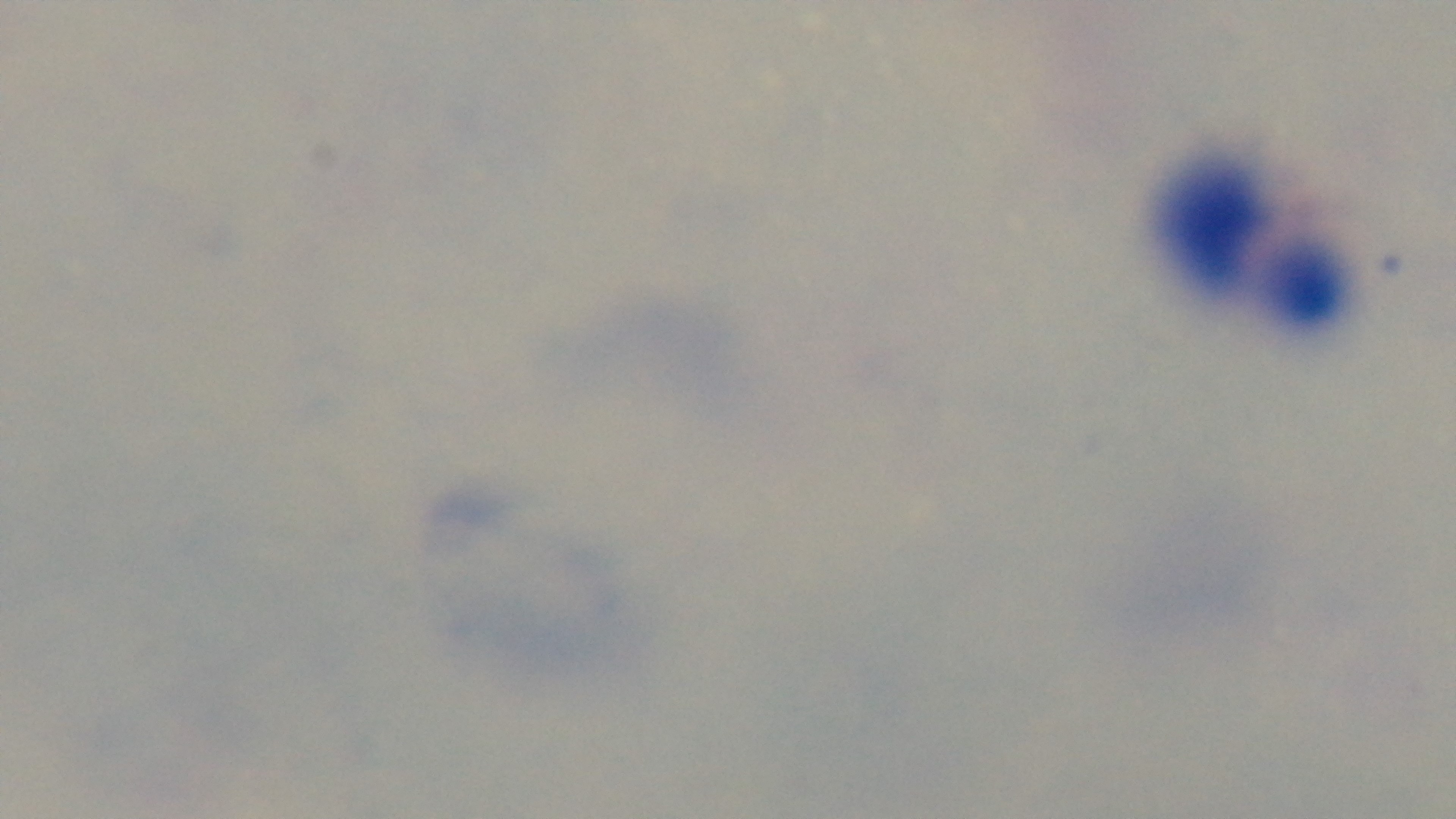

Giemsa-stained. Oil-immersion objective, 100x. Preparation: thick. Malaria status: negative. Photomicrograph. One field from the slide. Mounted 4K digital camera.